Describe the morphology of the erythrocytes.
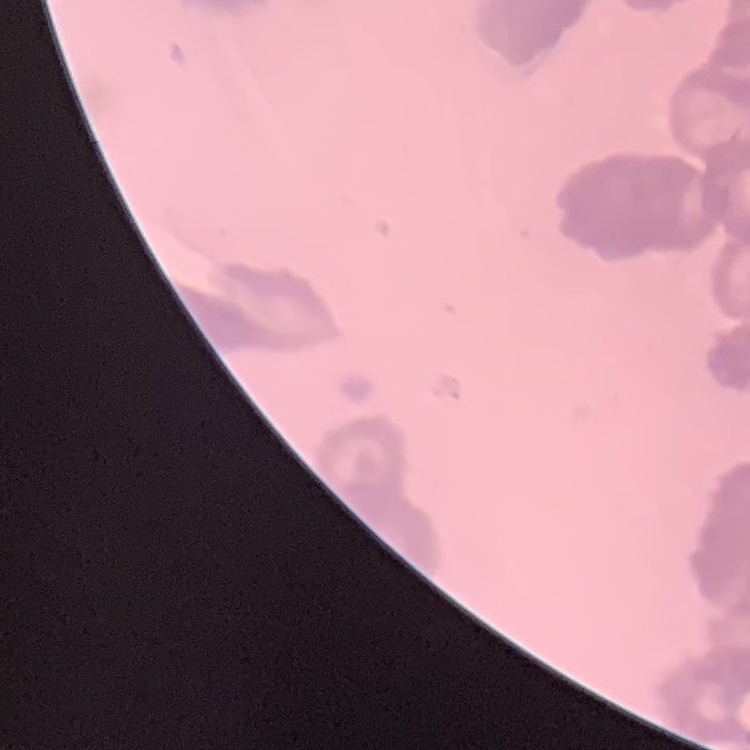

They show rouleaux formation.

One tile cut from a larger photomicrograph. Field's or Giemsa stain. Thin blood smear.